Identify the cell.
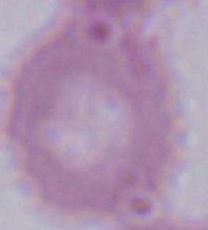
This is an erythrocyte.

1000x magnification. Micrograph.